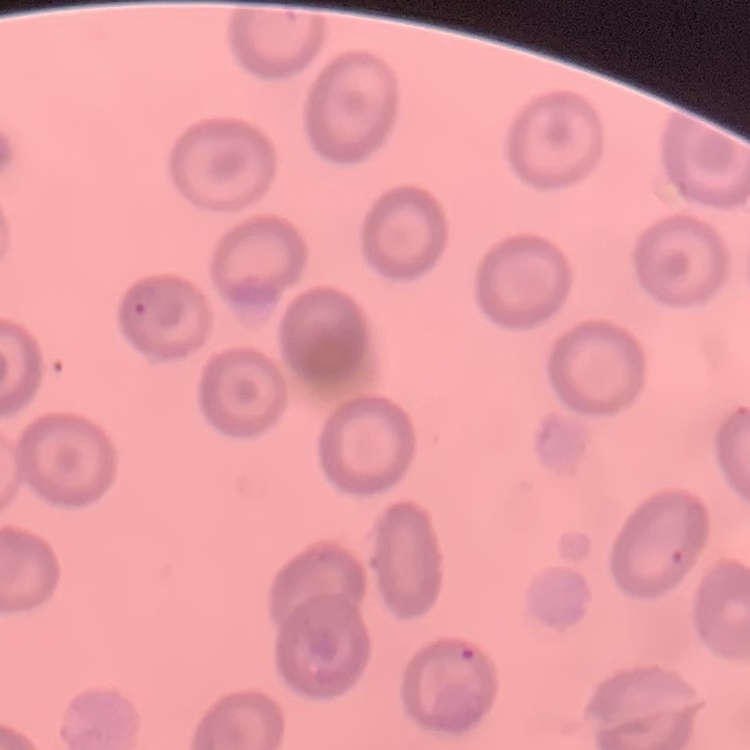

{
  "erythrocyte_morphology": "no rouleaux formation",
  "stain": "Field's or Giemsa",
  "preparation": "thin blood smear",
  "image_type": "square crop of a larger photomicrograph"
}